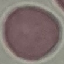
result = no malaria parasites seen
stain = Giemsa
capture = smartphone camera at the microscope eyepiece
preparation = thin blood film
image type = automatically extracted cell patch, resized to 64 × 64 pixels